State the blood parasite species.
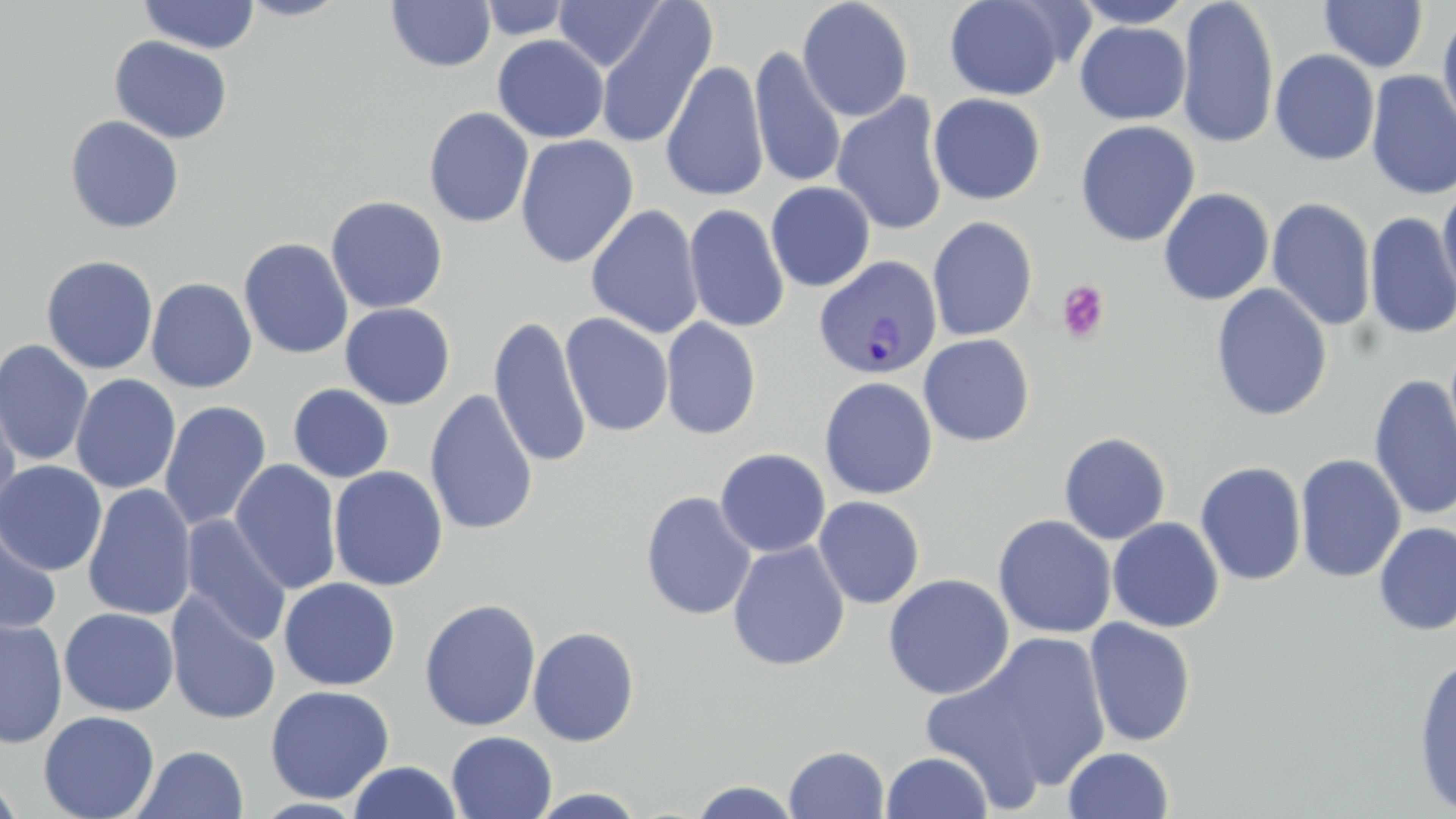
Plasmodium vivax.

modality = light microscopy
magnification = 1000x
platelet locations = approximate bounding boxes as (x1,y1)-(x2,y2) corner pairs in pixels: (1056,280)-(1111,343)
uninfected red blood cell locations = approximate bounding boxes as (x1,y1)-(x2,y2) corner pairs in pixels: (236,0)-(352,21), (386,0)-(496,72), (478,0)-(575,40), (553,0)-(667,72), (797,0)-(914,122), (943,0)-(1070,101), (1072,0)-(1195,28), (1176,0)-(1279,149), (1319,0)-(1428,72), (138,1)-(261,54), (594,2)-(717,151), (1437,8)-(1456,139), (1075,21)-(1191,125), (492,34)-(609,144), (109,36)-(233,144), (749,46)-(847,189), (1269,49)-(1380,166), (660,60)-(769,203), (1366,70)-(1456,201), (831,92)-(949,236), (928,93)-(1046,206), (423,106)-(535,228), (64,114)-(185,233), (1074,120)-(1200,247), (515,134)-(638,269), (1438,178)-(1456,306), (766,182)-(876,292), (1158,188)-(1274,305), (326,195)-(448,313), (1266,197)-(1377,332), (684,203)-(790,333), (586,204)-(704,338), (1364,212)-(1456,340), (927,215)-(1038,341), (238,237)-(354,359), (41,255)-(159,374), (146,277)-(258,393), (1210,283)-(1332,421), (340,302)-(455,409), (560,312)-(674,437), (488,315)-(591,470), (660,317)-(761,440), (918,334)-(1035,446), (0,339)-(94,466), (70,374)-(181,494), (1368,374)-(1456,522), (819,377)-(938,500), (288,384)-(394,483), (0,387)-(21,525), (424,388)-(539,536), (160,401)-(271,531), (1058,431)-(1171,545), (715,447)-(831,558), (1294,453)-(1406,583), (229,459)-(343,594), (0,460)-(107,576), (1195,461)-(1307,586), (328,465)-(448,591), (83,483)-(197,622), (640,490)-(757,621), (813,496)-(925,609), (993,514)-(1116,639), (180,516)-(292,646), (1107,517)-(1224,633), (1,521)-(61,636), (1374,522)-(1456,635), (728,540)-(849,671), (882,573)-(1015,700), (278,577)-(401,690), (164,591)-(282,726), (419,598)-(541,732), (59,607)-(179,716), (0,618)-(68,748), (1083,618)-(1197,747), (528,626)-(640,746), (928,631)-(1114,803), (1412,654)-(1456,816), (265,684)-(395,804), (38,710)-(159,819), (446,730)-(557,819), (132,745)-(248,819), (783,745)-(890,819), (1063,746)-(1174,819), (880,751)-(993,819), (348,761)-(463,818), (0,771)-(24,819), (687,780)-(804,818), (527,788)-(650,818)
stain = May-Grünwald-Giemsa
image size = 1456×819 pixels
preparation = thin blood film
field of view = one of a larger specimen
Plasmodium vivax-infected red blood cell locations = approximate bounding boxes as (x1,y1)-(x2,y2) corner pairs in pixels: (813,255)-(943,379)